Locate every Plasmodium parasite and every leukocyte.
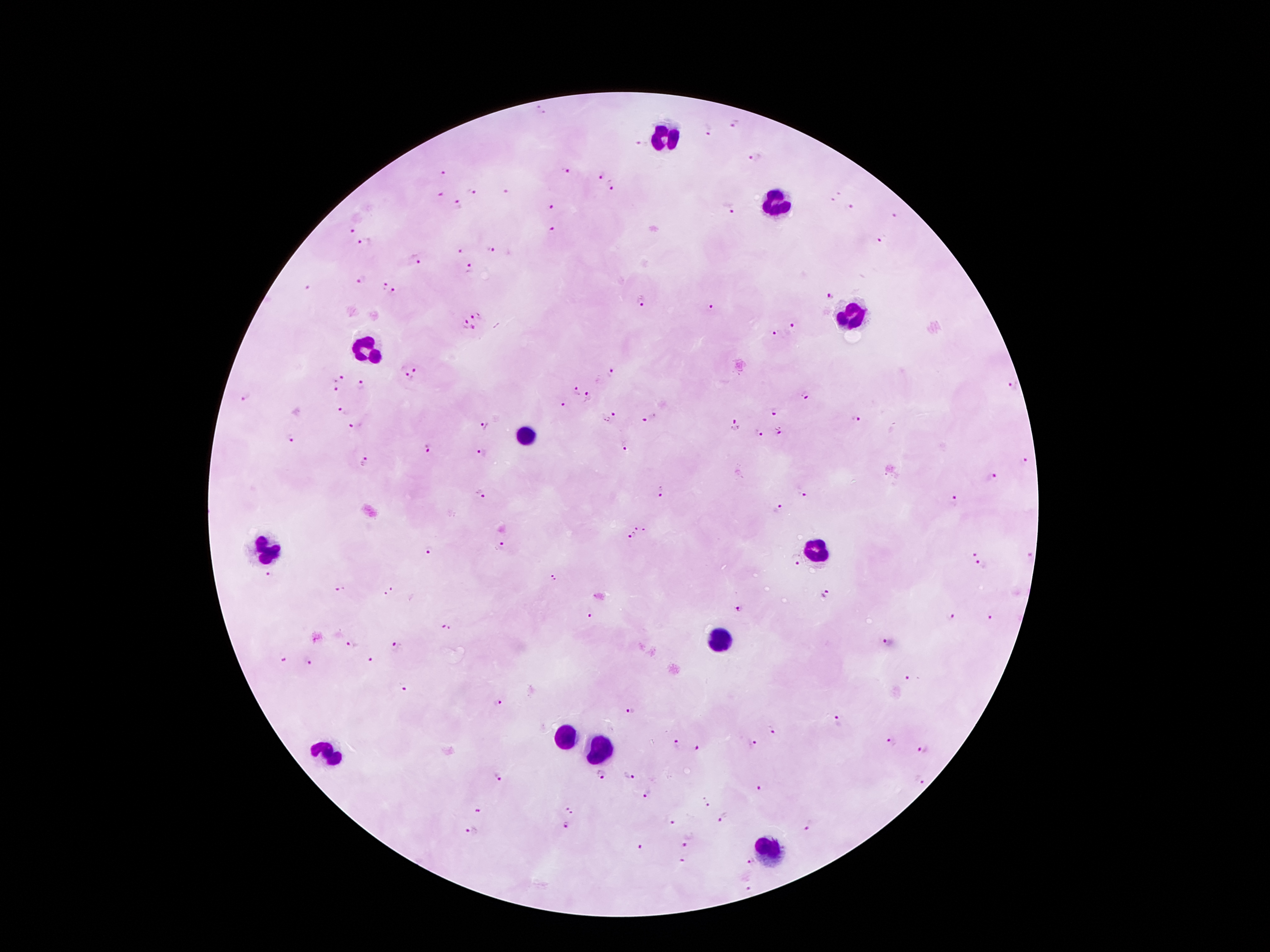

Approximate centers as (x, y) in pixels.
Plasmodium parasites: (541, 110), (734, 124), (708, 129), (639, 146), (755, 157), (564, 171), (443, 173), (600, 177), (612, 187), (470, 192), (506, 192), (837, 193), (441, 194), (833, 200), (458, 206), (549, 207), (850, 208), (733, 209), (895, 216), (351, 231), (554, 231), (363, 241), (880, 242), (490, 249), (458, 251), (416, 261), (470, 268), (361, 280), (381, 286), (306, 287), (395, 292), (830, 297), (641, 300), (711, 307), (475, 316), (464, 324), (792, 326), (472, 329), (777, 333), (415, 369), (612, 373), (406, 378), (340, 379), (361, 386), (1012, 386), (336, 389), (576, 391), (805, 396), (245, 398), (589, 398), (564, 405), (343, 411), (774, 412), (615, 413), (856, 418), (648, 419), (606, 420), (352, 424), (483, 425), (734, 425), (780, 431), (758, 434), (290, 439), (626, 445), (427, 449), (482, 452), (1025, 459), (364, 463), (989, 476), (661, 492), (481, 494), (804, 494), (952, 501), (777, 507), (634, 527), (646, 532), (629, 538), (501, 546), (428, 549), (974, 552), (1029, 556), (795, 560), (982, 566), (269, 573), (553, 576), (340, 590), (390, 591), (827, 592), (740, 608), (590, 614), (948, 616), (991, 616), (446, 628), (889, 642), (351, 645), (396, 648), (282, 658), (310, 660), (371, 662), (907, 677), (403, 685), (497, 704), (630, 711), (839, 722), (771, 728), (893, 742), (752, 743), (677, 744), (923, 748), (698, 749), (602, 774), (627, 776), (499, 777), (919, 779), (761, 788), (648, 792), (705, 803), (570, 809), (478, 811), (725, 816), (673, 821), (812, 825), (565, 827), (471, 832), (687, 842), (639, 847), (681, 861), (751, 862), (747, 884).
Leukocytes: (666, 139), (776, 204), (846, 314), (370, 348), (526, 434), (261, 550), (815, 550), (715, 644), (567, 734), (602, 751), (328, 755), (766, 852).

Photographed through the microscope eyepiece with a smartphone camera. Single field of view. Patient malaria status: infected with Plasmodium falciparum. Giemsa stain. Thick peripheral-blood smear. Image is 1270×952 pixels. 100x magnification.